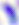
Summary:
  - Modality: photomicrograph
  - Identification: Toxoplasma gondii
  - Magnification: 400x